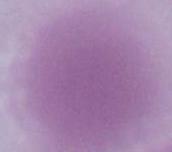

Summary:
  - Modality: micrograph
  - Magnification: 1000x
  - Identification: erythrocyte